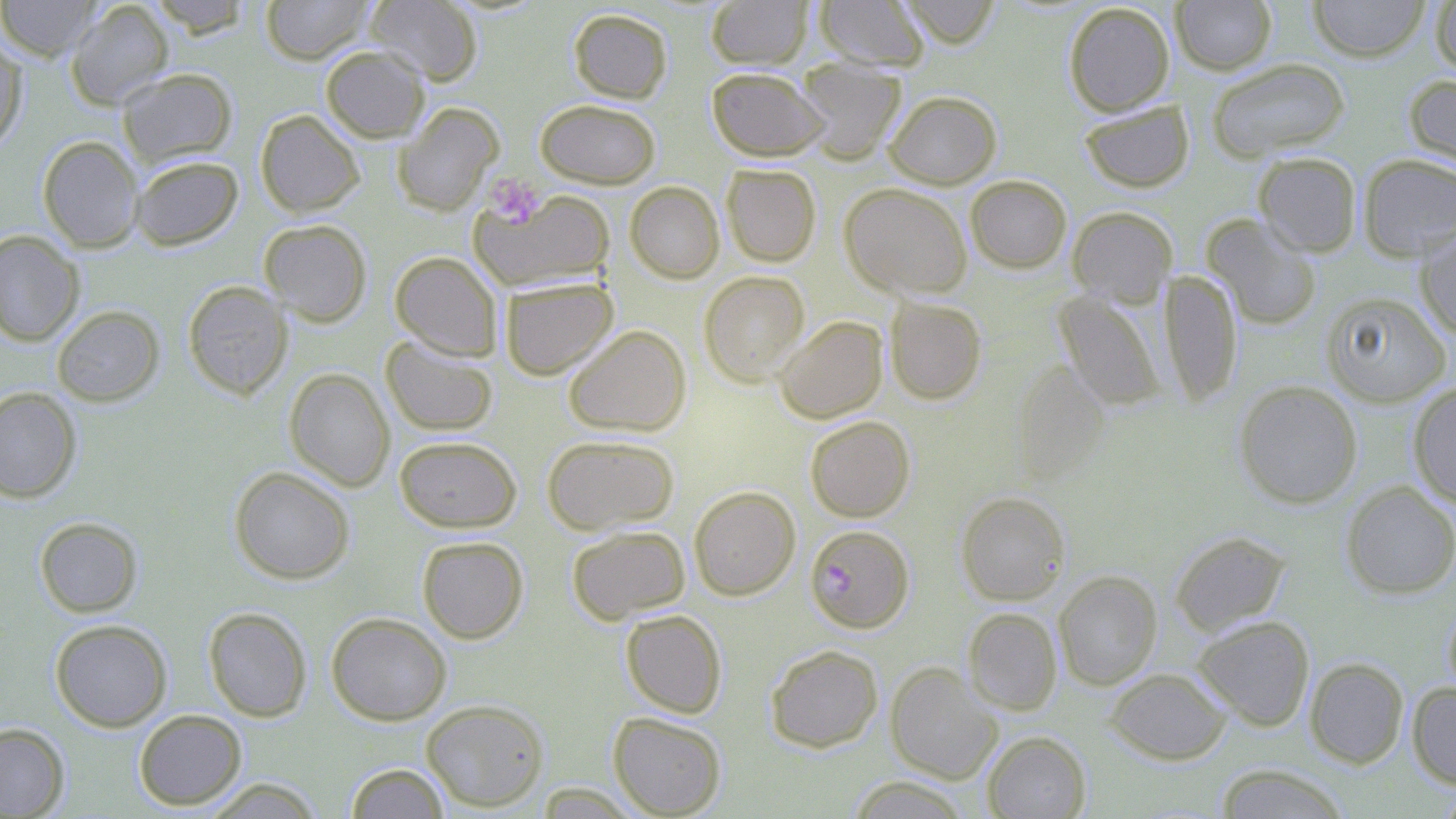
{
  "slide_level_diagnosis": "Plasmodium falciparum",
  "image_size": "1456×819 pixels",
  "magnification": "1000x",
  "modality": "light microscopy",
  "field_of_view": "one of a larger specimen",
  "stain": "May-Grünwald-Giemsa",
  "platelet_locations": "approximate bounding boxes as [x1, y1, x2, y2] in pixels: [484, 173, 545, 227]",
  "plasmodium_falciparum_infected_red_blood_cell_locations": "approximate bounding boxes as [x1, y1, x2, y2] in pixels: [805, 524, 914, 633]",
  "preparation": "thin blood smear",
  "uninfected_red_blood_cell_locations": "approximate bounding boxes as [x1, y1, x2, y2] in pixels: [0, 0, 102, 61], [145, 0, 256, 38], [260, 0, 373, 64], [365, 0, 482, 85], [813, 0, 930, 72], [897, 0, 1001, 48], [1171, 0, 1276, 75], [1308, 0, 1431, 62], [1429, 0, 1456, 79], [65, 1, 175, 110], [706, 1, 812, 69], [1063, 2, 1175, 116], [568, 8, 673, 103], [0, 31, 28, 151], [320, 45, 429, 142], [1206, 58, 1350, 162], [794, 60, 907, 164], [117, 67, 238, 167], [706, 67, 828, 161], [1403, 73, 1456, 180], [884, 90, 1002, 189], [535, 99, 661, 188], [1079, 100, 1194, 192], [393, 102, 504, 216], [255, 109, 365, 217], [37, 135, 144, 253], [1253, 151, 1362, 257], [1357, 154, 1456, 262], [130, 155, 243, 250], [721, 164, 821, 267], [965, 174, 1072, 273], [625, 181, 724, 283], [839, 183, 973, 300], [470, 187, 615, 292], [1067, 206, 1177, 308], [1201, 213, 1322, 330], [260, 219, 372, 326], [1415, 225, 1456, 339], [0, 230, 85, 346], [390, 251, 502, 360], [1159, 270, 1243, 409], [698, 271, 810, 387], [499, 277, 618, 380], [182, 280, 293, 399], [1053, 291, 1166, 411], [1321, 291, 1452, 407], [884, 298, 987, 404], [52, 305, 165, 407], [774, 315, 888, 423], [563, 324, 691, 437], [381, 336, 498, 437], [1012, 362, 1110, 486], [284, 368, 395, 491], [1233, 379, 1363, 509], [1408, 382, 1456, 507], [0, 387, 82, 503], [805, 415, 915, 522], [541, 434, 680, 535], [394, 435, 522, 532], [229, 466, 355, 584], [1340, 481, 1456, 599], [688, 485, 801, 600], [955, 491, 1070, 605], [34, 517, 143, 617], [566, 524, 690, 624], [1169, 530, 1290, 636], [416, 536, 529, 643], [1053, 571, 1162, 690], [1443, 600, 1456, 704], [203, 606, 313, 722], [963, 607, 1062, 715], [620, 609, 727, 718], [326, 611, 452, 725], [1193, 615, 1315, 730], [50, 619, 172, 731], [765, 644, 883, 752], [1304, 657, 1408, 768], [885, 662, 1003, 784], [1105, 667, 1231, 764], [1407, 682, 1456, 790], [421, 699, 549, 811], [133, 709, 247, 810], [608, 711, 726, 817], [0, 722, 69, 817], [983, 731, 1091, 818], [345, 762, 450, 819], [1214, 763, 1350, 819], [846, 776, 971, 818], [203, 778, 325, 818], [1432, 786, 1456, 818]"
}